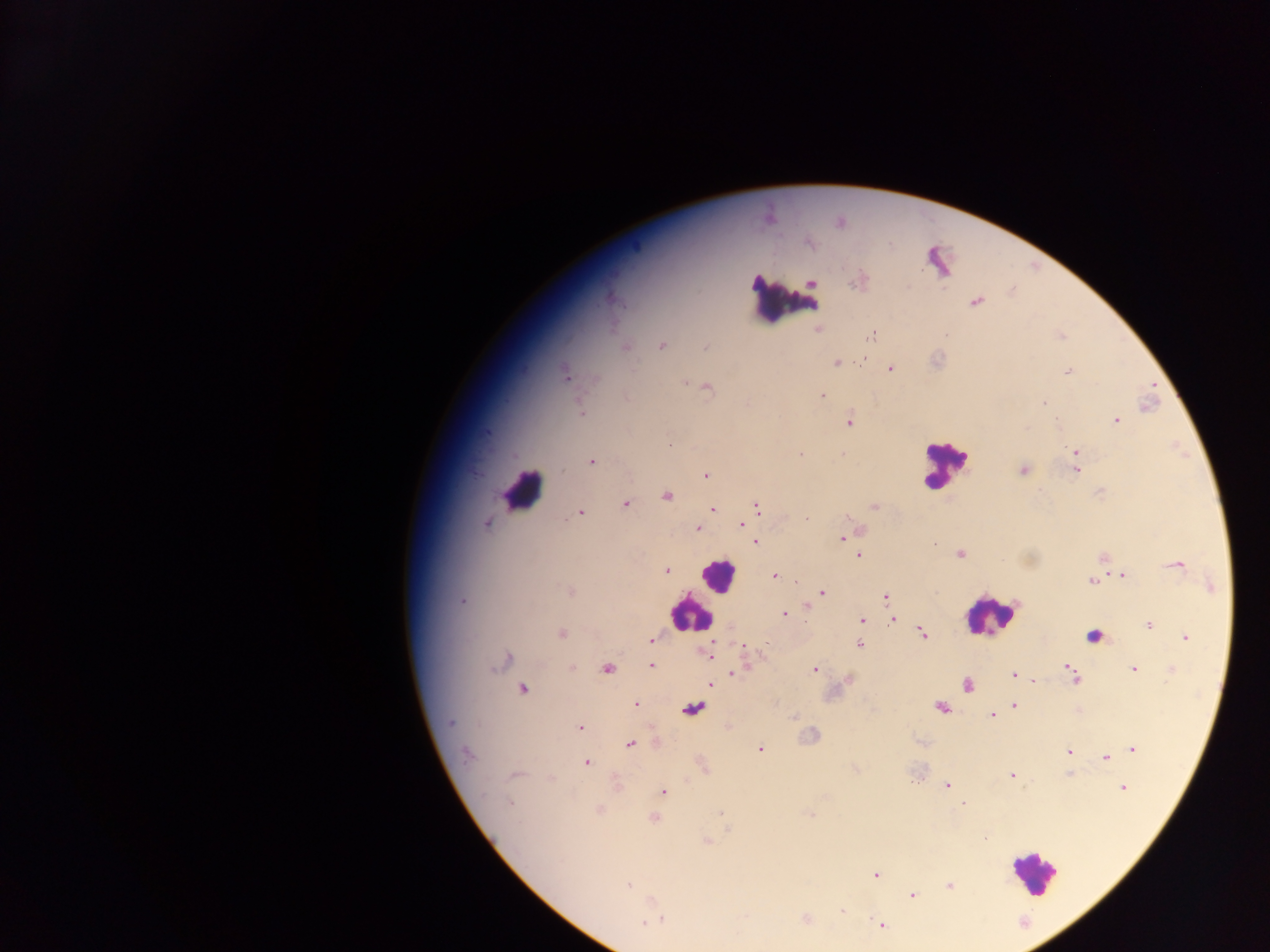

Approximate centers as {x, y} in pixels.
Summary:
  - Malaria parasite locations: {976, 301}, {818, 328}, {872, 335}, {661, 346}, {624, 347}, {706, 347}, {836, 362}, {890, 367}, {1068, 372}, {565, 373}, {687, 383}, {705, 387}, {822, 395}, {1042, 401}, {581, 413}, {849, 420}, {1116, 420}, {1075, 450}, {798, 454}, {842, 454}, {591, 462}, {1076, 469}, {1023, 470}, {705, 475}, {666, 495}, {624, 504}, {874, 506}, {756, 507}, {712, 509}, {580, 512}, {806, 518}, {486, 523}, {742, 524}, {697, 528}, {843, 537}, {755, 542}, {933, 544}, {959, 554}, {858, 555}, {1104, 558}, {1175, 565}, {667, 570}, {1123, 574}, {773, 576}, {1091, 581}, {1211, 586}, {569, 591}, {822, 592}, {886, 597}, {462, 600}, {806, 608}, {783, 614}, {861, 619}, {893, 619}, {1148, 625}, {561, 633}, {921, 633}, {1185, 638}, {651, 640}, {859, 644}, {743, 647}, {708, 653}, {503, 660}, {651, 665}, {1069, 666}, {572, 668}, {606, 668}, {814, 669}, {1134, 669}, {1171, 670}, {733, 671}, {1014, 676}, {1074, 678}, {849, 679}, {1033, 680}, {710, 684}, {967, 684}, {521, 688}, {1013, 700}, {635, 704}, {1014, 705}, {941, 708}, {692, 709}, {993, 715}, {794, 717}, {727, 725}, {580, 727}, {656, 740}, {629, 744}, {1131, 748}, {759, 749}, {1068, 752}, {467, 754}, {1105, 757}, {586, 762}, {702, 766}, {1067, 773}, {515, 775}, {1011, 775}, {617, 785}, {947, 786}, {1122, 787}, {662, 791}, {510, 802}, {963, 804}, {599, 811}, {653, 818}, {707, 841}, {876, 875}, {628, 884}, {948, 885}, {911, 894}, {842, 910}, {657, 916}, {805, 918}, {649, 920}, {881, 925}
  - Leukocyte locations: {783, 300}, {944, 464}, {522, 491}, {718, 576}, {690, 613}, {991, 614}, {1094, 633}, {1034, 872}
  - Country: Ghana
  - Preparation: thick blood film
  - Field of view: single
  - Capture: mobile-phone photograph through a microscope
  - Image size: 1270×952 pixels